Name the blood parasite species.
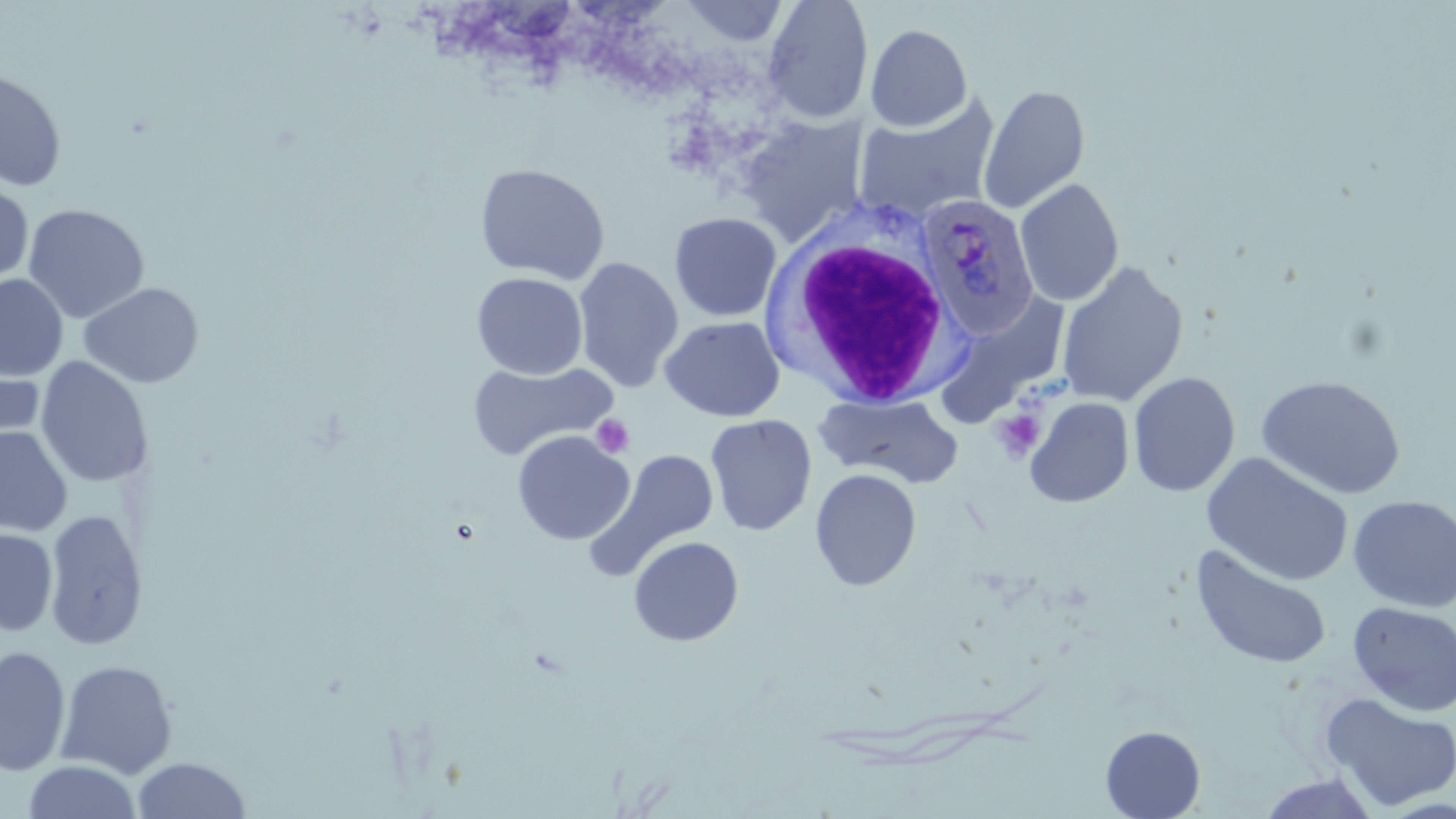
Plasmodium ovale.

field_of_view: one of a larger specimen
magnification: 1000x
plasmodium_ovale_infected_red_blood_cell_locations: 'approximate bounding boxes as [x1, y1, x2, y2] in pixels: [916, 195, 1039, 338]'
platelet_locations: 'approximate bounding boxes as [x1, y1, x2, y2] in pixels: [992, 408, 1046, 461], [591, 414, 635, 459]'
modality: light microscopy
preparation: thin blood smear
stain: May-Grünwald-Giemsa
image_size: 1456×819 pixels
white_blood_cell_locations: 'approximate bounding boxes as [x1, y1, x2, y2] in pixels: [761, 204, 967, 411]'
uninfected_red_blood_cell_locations: 'approximate bounding boxes as [x1, y1, x2, y2] in pixels: [762, 0, 873, 124], [680, 1, 790, 46], [865, 24, 973, 131], [0, 69, 67, 192], [979, 84, 1090, 214], [854, 96, 1000, 225], [735, 115, 867, 247], [473, 163, 610, 285], [1014, 178, 1124, 307], [0, 185, 34, 284], [23, 204, 150, 324], [669, 213, 782, 322], [573, 258, 684, 392], [1056, 261, 1189, 407], [471, 272, 588, 379], [0, 274, 68, 381], [78, 282, 205, 389], [933, 293, 1072, 428], [660, 315, 786, 422], [0, 352, 44, 456], [35, 356, 154, 490], [467, 360, 618, 463], [1128, 372, 1241, 497], [1256, 375, 1407, 500], [815, 392, 964, 489], [1025, 396, 1134, 508], [705, 414, 817, 536], [0, 426, 73, 537], [512, 430, 634, 545], [587, 449, 722, 578], [1202, 452, 1354, 587], [810, 468, 922, 591], [1348, 494, 1456, 613], [44, 507, 148, 651], [0, 528, 58, 635], [628, 536, 744, 646], [1190, 544, 1332, 670], [1348, 601, 1456, 717], [0, 645, 71, 777], [56, 659, 178, 779], [1320, 692, 1456, 812], [1100, 726, 1205, 819], [131, 757, 251, 818], [24, 760, 141, 818], [1254, 772, 1381, 817]'